Report the malaria status of this cell.
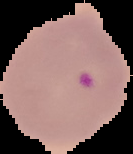
It is parasitized.

image_size: 133×154 pixels
image_type: cell region segmented out of the field of view; surrounding area masked to black
preparation: thin blood smear